Give the position of every leukocyte visible.
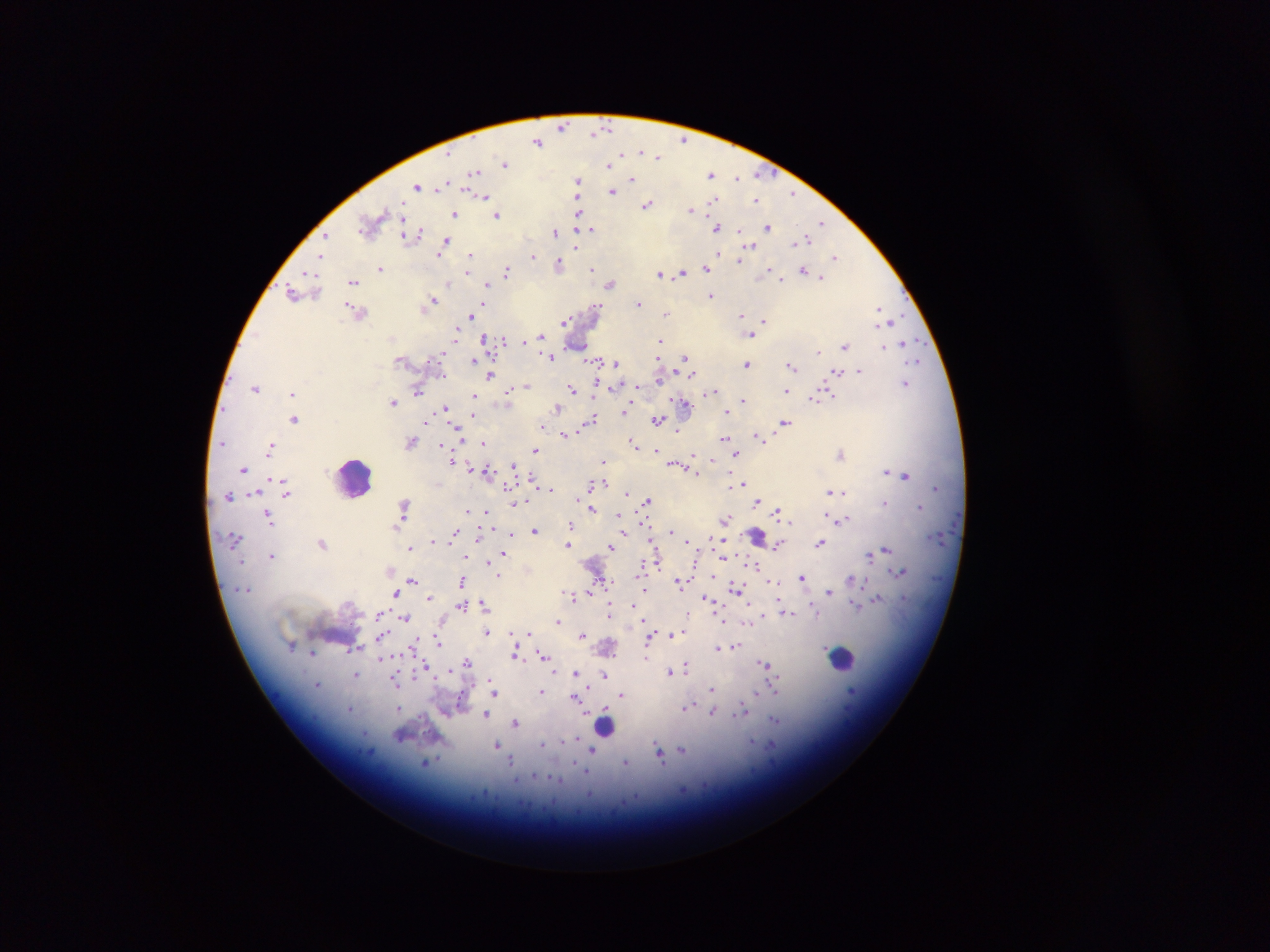
Approximate centers as x y in pixels.
Leukocytes: 354 476; 757 535; 843 659; 606 726.

Summary:
  - Malaria parasite locations: 562 126; 598 131; 683 140; 537 142; 649 152; 658 155; 505 163; 610 164; 475 172; 758 172; 711 175; 737 177; 632 178; 578 181; 445 183; 418 185; 613 190; 793 193; 485 196; 578 196; 715 201; 756 201; 648 204; 691 210; 455 215; 497 215; 580 215; 371 223; 821 223; 717 225; 768 226; 591 228; 556 232; 412 233; 326 238; 804 238; 446 241; 576 244; 749 246; 719 253; 438 255; 470 255; 741 255; 321 256; 533 256; 835 256; 740 261; 559 264; 381 268; 706 268; 592 269; 803 270; 507 271; 683 272; 468 273; 660 273; 667 273; 310 276; 821 278; 781 279; 353 280; 448 282; 488 282; 610 284; 294 293; 711 296; 432 299; 640 303; 598 307; 879 309; 357 311; 475 312; 666 313; 471 315; 741 315; 891 320; 764 321; 564 322; 456 331; 751 334; 542 336; 485 339; 504 340; 660 340; 904 343; 846 344; 579 346; 882 346; 819 350; 441 353; 549 356; 686 359; 474 360; 594 361; 918 361; 615 362; 747 363; 792 364; 859 369; 837 371; 491 375; 660 378; 597 382; 906 382; 527 385; 638 386; 255 387; 572 387; 419 388; 511 389; 292 391; 713 392; 788 392; 474 394; 820 395; 814 399; 743 400; 394 402; 630 403; 684 403; 557 407; 446 408; 626 410; 726 410; 473 416; 295 418; 591 420; 658 420; 784 422; 427 423; 543 424; 458 427; 678 431; 564 433; 758 436; 724 438; 412 442; 222 443; 481 443; 635 443; 271 445; 441 445; 656 448; 535 449; 736 454; 841 454; 694 456; 710 459; 454 461; 604 462; 513 465; 676 465; 244 469; 695 470; 487 471; 886 471; 906 475; 278 480; 605 483; 743 483; 591 485; 739 485; 509 486; 550 487; 936 488; 831 491; 842 492; 286 494; 627 494; 229 496; 648 501; 758 501; 885 503; 513 504; 404 506; 919 507; 592 509; 468 511; 487 512; 779 512; 619 514; 268 515; 829 515; 400 519; 724 519; 842 519; 642 522; 572 524; 535 531; 671 531; 455 533; 511 533; 480 536; 713 537; 432 540; 686 541; 821 542; 323 543; 569 545; 777 545; 610 547; 410 548; 725 548; 886 550; 504 553; 870 554; 272 555; 724 555; 463 556; 489 562; 696 562; 756 565; 900 571; 713 573; 498 575; 803 576; 854 579; 412 580; 607 580; 680 581; 775 581; 462 582; 737 588; 645 590; 829 591; 396 592; 590 592; 566 593; 572 596; 430 598; 707 598; 877 598; 483 603; 857 604; 462 605; 634 605; 812 608; 379 613; 609 613; 786 613; 687 615; 764 615; 405 617; 724 620; 558 621; 748 621; 685 630; 487 631; 528 632; 381 633; 671 634; 583 635; 650 637; 439 641; 414 642; 735 645; 718 646; 516 652; 312 653; 543 655; 647 657; 382 659; 467 662; 766 664; 687 665; 426 666; 449 670; 670 671; 555 672; 575 672; 357 674; 604 675; 489 677; 395 680; 713 688; 586 689; 542 691; 775 691; 494 692; 852 692; 759 694; 622 695; 577 696; 686 706; 400 708; 352 709; 742 711; 713 712; 486 713; 775 719; 516 723; 752 741; 773 744; 497 745; 592 749; 683 750; 660 754; 511 760; 625 762; 427 763
  - Image size: 1270×952 pixels
  - Field of view: single
  - Capture: mobile-phone photograph through a microscope
  - Country: Ghana
  - Preparation: thick blood smear